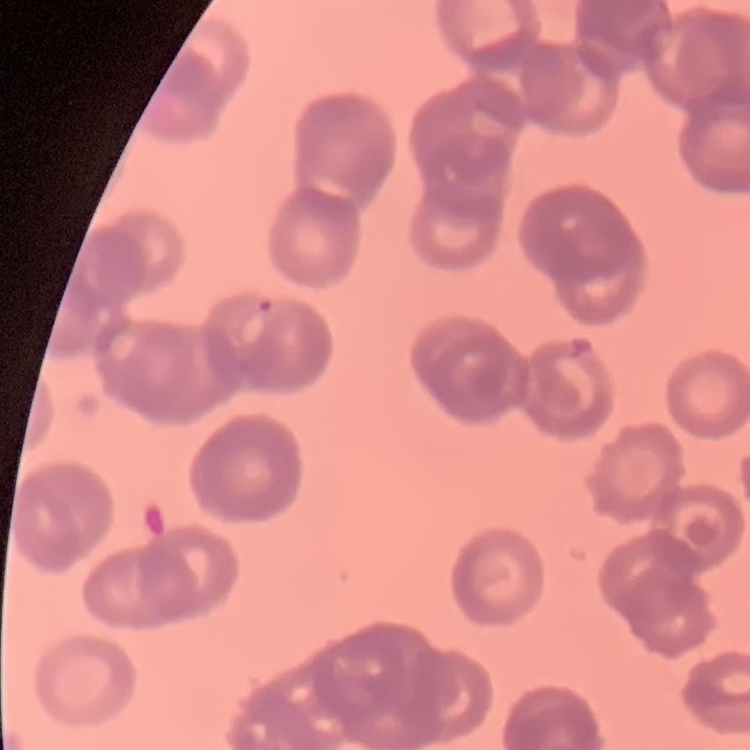
Summary:
  - Erythrocyte morphology: rouleaux formation
  - Stain: Field's or Giemsa
  - Preparation: thin peripheral smear
  - Image type: one tile cut from a larger photomicrograph